Assess this cell for malaria.
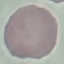
It is uninfected.

stain = Giemsa
preparation = thin smear
capture = smartphone through the microscope eyepiece
image type = automatically extracted cell patch, resized to 64 × 64 pixels